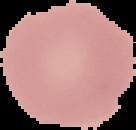 Image is 136×130 pixels. Cell region segmented out of the field of view; the surrounding area is masked to black. From a thin blood smear. Malaria status: uninfected.